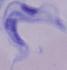
magnification = 1000x
identification = trypanosome
modality = micrograph